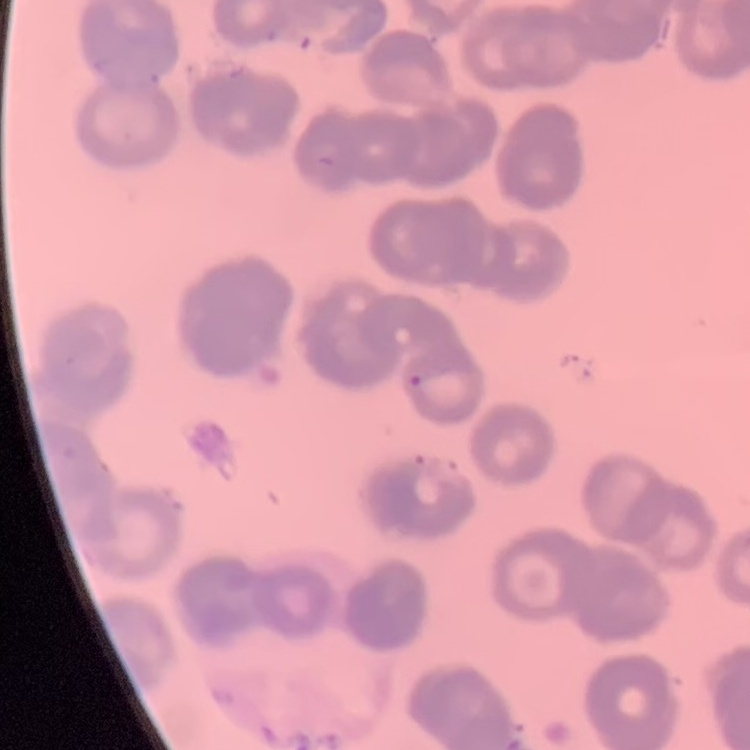
The red blood cells exhibit rouleaux formation. Stained with either Field's or Giemsa. One tile cut from a larger photomicrograph. Thin peripheral smear.